Assess this cell for malaria.
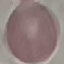
It is uninfected.

capture = smartphone through the microscope eyepiece
image type = automatically extracted cell patch, resized to 64 × 64 pixels
stain = Giemsa
preparation = thin blood film